Outline each blood parasite and name the species.
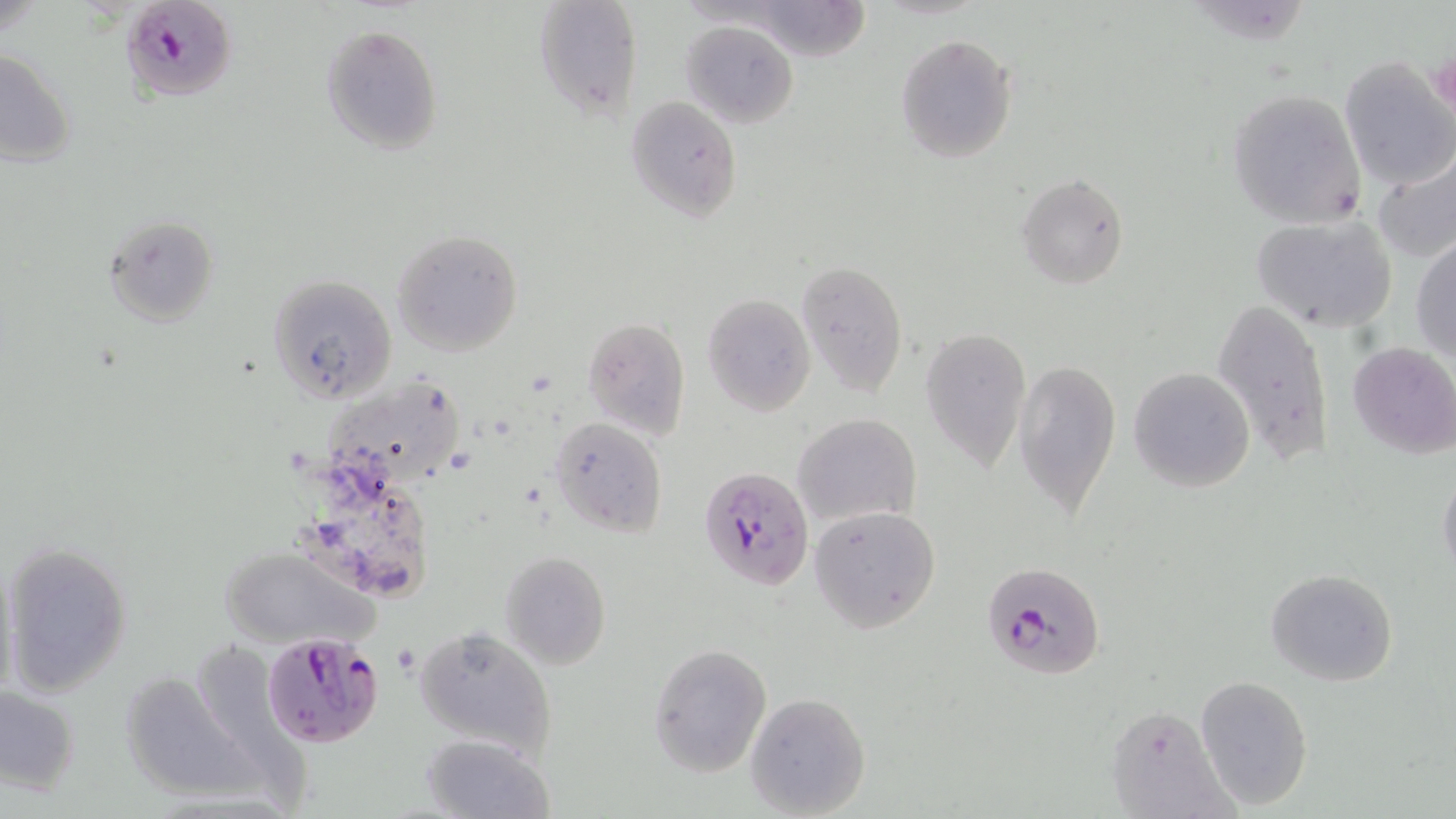
Approximate bounding boxes as (x1,y1)-(x2,y2) corner pairs in pixels.
Plasmodium falciparum-infected red blood cells: (120,1)-(236,101), (699,466)-(814,593), (980,560)-(1104,680), (259,632)-(385,748).
No Plasmodium ovale, Plasmodium malariae, Plasmodium vivax, Babesia divergens, or Trypanosoma brucei observed.

Uninfected red blood cell locations: (532,0)-(643,120), (750,1)-(871,62), (682,19)-(798,127), (321,24)-(444,155), (894,34)-(1018,163), (1,47)-(76,168), (1340,59)-(1454,189), (1226,89)-(1367,231), (625,95)-(742,222), (1373,151)-(1455,266), (1016,174)-(1128,287), (1251,214)-(1399,333), (105,215)-(218,325), (392,230)-(523,356), (1411,233)-(1456,365), (796,261)-(906,396), (269,275)-(396,404), (702,294)-(816,417), (1211,295)-(1335,465), (581,317)-(690,441), (919,324)-(1031,471), (1349,341)-(1456,458), (1014,358)-(1119,519), (1128,366)-(1256,493), (331,371)-(461,481), (794,412)-(920,527), (550,416)-(667,536), (1438,466)-(1456,581), (810,506)-(942,632), (0,540)-(134,697), (218,547)-(375,649), (499,551)-(610,671), (1265,568)-(1397,686), (414,625)-(557,761), (649,642)-(773,777), (118,669)-(255,802), (1195,674)-(1313,809), (1,685)-(81,796), (744,692)-(870,818), (1105,704)-(1236,819), (422,733)-(554,818). Slide-level diagnosis: Plasmodium falciparum. Image is 1456×819 pixels. Thin blood film. Captured at 1000x magnification. Single field of view. Optical microscopy. May-Grünwald-Giemsa-stained preparation.